Assess this cell for malaria.
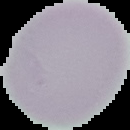

Uninfected.

Summary:
  - Image type: segmented cell region with the area outside set to black
  - Image size: 130×130 pixels
  - Preparation: thin blood smear